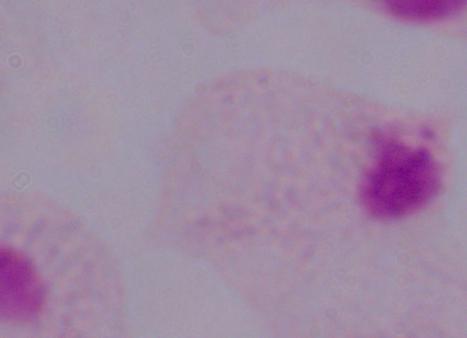
Summary:
  - Identification: trichomonad
  - Magnification: 1000x
  - Modality: photomicrograph